Assess this cell for malaria.
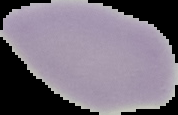
It is uninfected.

image_size: 178×115 pixels
preparation: thin blood film
image_type: segmented cell region on a black background